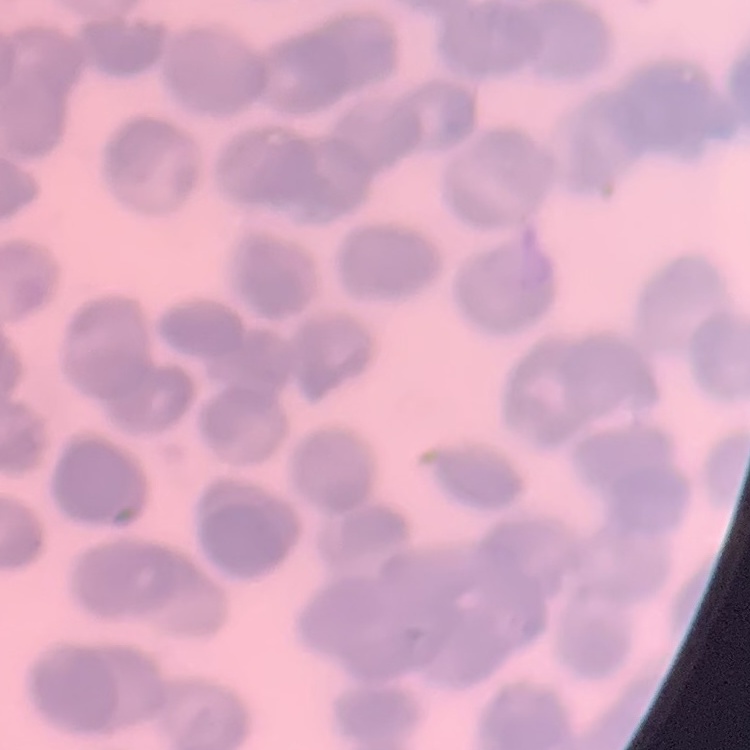

erythrocyte morphology = rouleaux formation
image type = one tile cut from a larger photomicrograph
stain = Field's or Giemsa
preparation = thin blood film